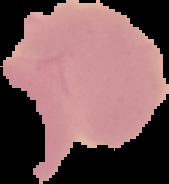 Cell region segmented out of the field of view; the surrounding area is masked to black. Image is 169×184 pixels. Result: negative for Plasmodium parasites. From a thin blood film.